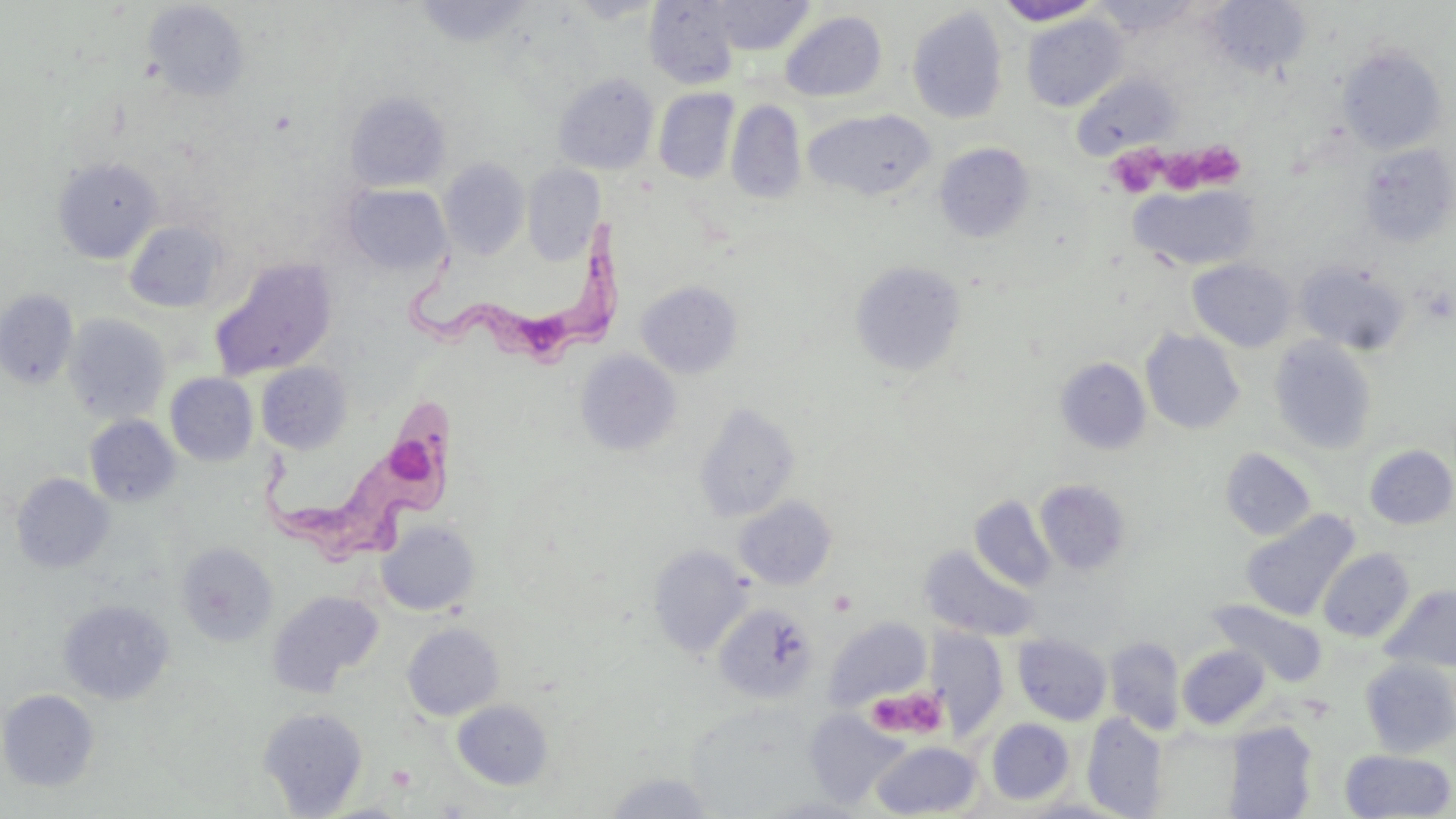
Summary:
  - Coordinate format: approximate bounding boxes as (x1,y1)-(x2,y2) corner pairs in pixels
  - Uninfected red blood cell locations: (566,0)-(665,24), (708,0)-(815,55), (143,1)-(250,101), (414,1)-(534,47), (644,1)-(741,88), (994,1)-(1105,26), (1087,1)-(1204,36), (1207,1)-(1311,77), (907,7)-(1008,125), (780,11)-(887,103), (1022,14)-(1128,111), (1337,45)-(1447,154), (553,72)-(659,174), (1072,73)-(1179,159), (653,88)-(739,184), (344,91)-(451,192), (727,100)-(806,205), (804,110)-(937,202), (934,143)-(1034,243), (1359,143)-(1455,247), (54,158)-(161,262), (440,158)-(530,260), (523,165)-(605,264), (343,183)-(451,275), (1131,183)-(1260,272), (124,221)-(228,313), (210,259)-(337,380), (1188,259)-(1297,351), (851,260)-(966,376), (1295,260)-(1411,355), (636,281)-(743,378), (0,290)-(79,390), (63,313)-(171,424), (1141,329)-(1245,435), (1269,337)-(1378,455), (575,350)-(682,456), (1055,357)-(1151,454), (256,362)-(352,453), (165,373)-(258,466), (694,402)-(801,522), (85,415)-(180,507), (1364,445)-(1456,529), (1220,447)-(1316,541), (11,473)-(114,574), (1035,479)-(1132,575), (734,496)-(837,589), (969,496)-(1056,591), (1240,509)-(1360,622), (376,519)-(480,616), (176,542)-(278,647), (647,545)-(753,658), (920,546)-(1038,641), (1318,548)-(1415,641), (1381,584)-(1456,673), (267,590)-(383,697), (58,599)-(174,705), (1209,599)-(1327,686), (714,603)-(819,704), (823,617)-(932,712), (402,622)-(504,720), (929,629)-(1008,739), (1013,634)-(1112,725), (1104,636)-(1186,736), (1177,644)-(1271,729), (1359,658)-(1456,757), (1,689)-(99,791), (452,699)-(554,790), (258,707)-(369,817), (803,709)-(909,809), (1082,713)-(1168,818), (986,718)-(1075,805), (1223,722)-(1318,818), (871,741)-(982,818), (1340,749)-(1454,818), (601,772)-(717,817), (755,795)-(877,818)
  - Trypanosoma brucei locations: (402,216)-(629,364), (256,399)-(469,566)
  - Platelet locations: (1109,144)-(1162,200), (1201,145)-(1244,191), (1162,151)-(1212,200), (865,685)-(949,741), (388,765)-(417,791)
  - Slide-level diagnosis: Trypanosoma brucei
  - Preparation: thin blood smear
  - Modality: light microscopy
  - Image size: 1456×819 pixels
  - Stain: May-Grünwald-Giemsa
  - Field of view: one of a larger specimen
  - Magnification: 1000x